Report the malaria status of this cell.
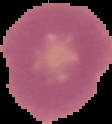

It is uninfected.

{
  "preparation": "thin blood film",
  "image_type": "segmented cell region on a black background",
  "image_size": "112×124 pixels"
}